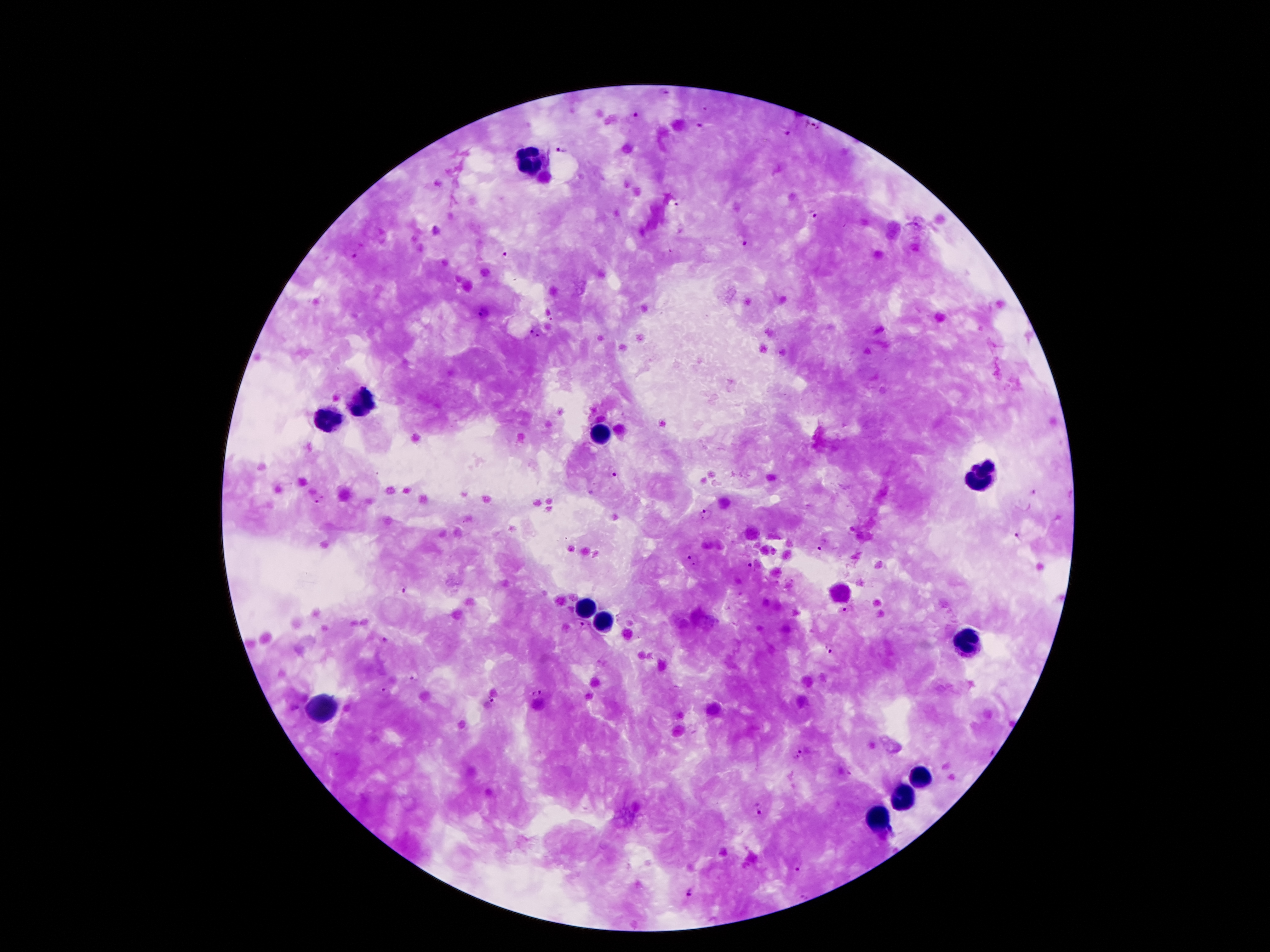 Approximate centers as (x, y) in pixels. Plasmodium parasite locations: (638, 116), (811, 123), (701, 125), (783, 133), (561, 149), (674, 204), (815, 213), (744, 239), (352, 251), (509, 256), (485, 311), (536, 334), (612, 471), (1032, 492), (318, 499), (706, 514), (1017, 536), (821, 545), (690, 559), (751, 567), (405, 590), (849, 608), (583, 625), (385, 641), (829, 650), (415, 678), (386, 691), (537, 694), (490, 700), (798, 754), (758, 810), (796, 867), (690, 892). Leukocyte locations: (529, 161), (364, 402), (328, 419), (599, 436), (975, 481), (585, 609), (602, 626), (969, 646), (319, 707), (919, 777), (905, 794), (877, 817). 100x magnification. Giemsa stain. Patient malaria status: positive for Plasmodium falciparum. Photographed through the microscope eyepiece with a smartphone camera. Single field of view. Thick peripheral-blood smear. Image is 1270×952 pixels.